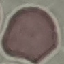

result = negative for malaria parasites
preparation = thin blood film
capture = smartphone camera at the microscope eyepiece
image type = cell patch, automatically extracted from a larger field of view and resized to 64 × 64 pixels
stain = Giemsa